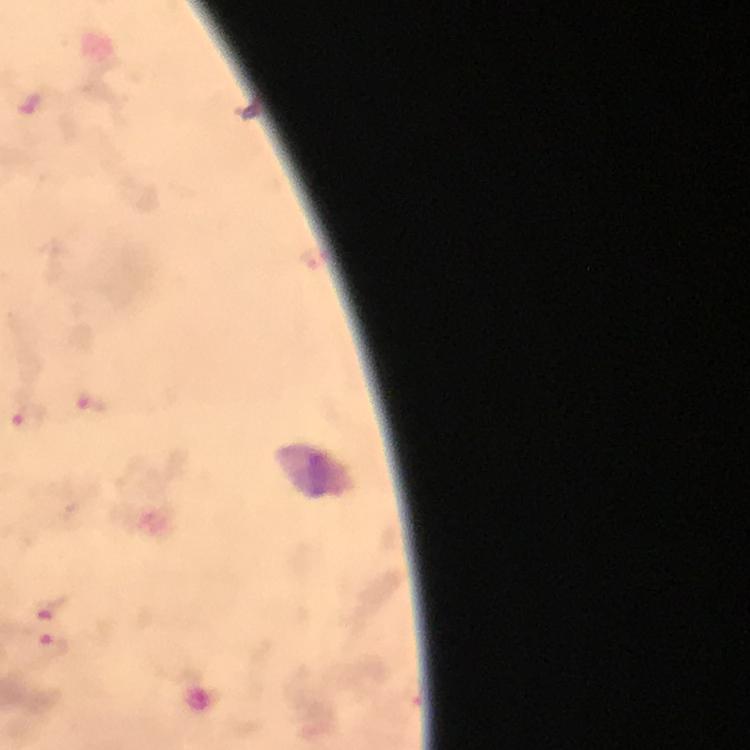

Approximate centers as (x, y) in pixels. Malaria parasite locations: (28, 102), (313, 258), (89, 403), (26, 418), (53, 608), (52, 648). Image is 750×750 pixels. Immersion oil was used. Thick blood smear. From a malaria diagnostic workup. Giemsa-stained preparation. 100x magnification. Photographed with a smartphone mounted on the microscope. Cropped region of a single field of view.